Identify the parasite.
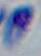

Toxoplasma gondii.

1000x magnification. Micrograph.